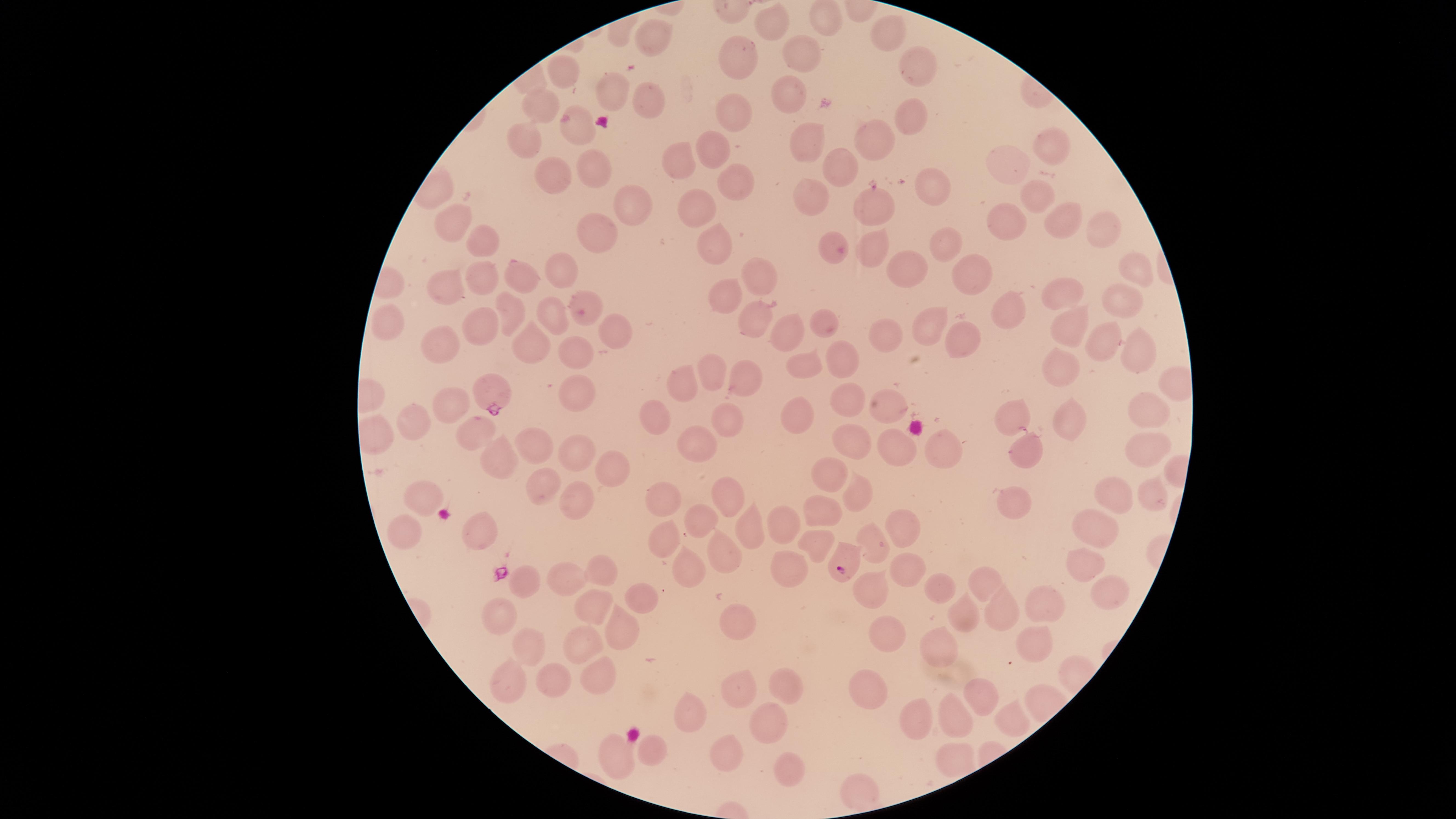

Approximate marker points as (x, y) in pixels. Uninfected red blood cells: (824, 21), (772, 27), (889, 35), (653, 37), (804, 59), (742, 61), (917, 64), (564, 77), (616, 93), (793, 100), (650, 102), (546, 106), (736, 115), (916, 119), (525, 135), (866, 135), (578, 136), (814, 141), (1050, 143), (715, 144), (681, 157), (838, 163), (1012, 164), (549, 167), (594, 167), (733, 179), (934, 185), (1036, 195), (628, 200), (812, 200), (704, 207), (881, 208), (1054, 217), (1008, 219), (457, 224), (1097, 231), (602, 232), (481, 239), (946, 239), (710, 245), (830, 249), (871, 249), (1140, 262), (909, 270), (565, 271), (973, 274), (526, 276), (753, 276), (480, 277), (449, 282), (728, 293), (1128, 294), (1064, 296), (582, 305), (512, 312), (1004, 313), (542, 316), (756, 320), (825, 323), (922, 324), (392, 326), (1068, 326), (474, 329), (613, 329), (783, 330), (963, 332), (884, 339), (1099, 340), (440, 341), (529, 346), (1132, 352), (581, 355), (845, 361), (810, 366), (1055, 373), (711, 374), (747, 376), (688, 387), (579, 395), (851, 397), (885, 405), (453, 409), (1152, 409), (799, 413), (659, 417), (1013, 419), (725, 421), (1066, 423), (417, 428), (475, 431), (850, 440), (938, 442), (698, 445), (1144, 446), (534, 449), (1026, 449), (576, 451), (898, 452), (501, 460), (609, 467), (835, 472), (728, 484), (543, 487), (866, 492), (1154, 494), (1112, 495), (581, 496), (423, 501), (662, 503), (826, 511), (1013, 511), (781, 522), (1100, 525), (702, 527), (482, 528), (750, 530), (405, 532), (898, 532), (885, 544), (821, 546), (668, 547), (726, 561), (1085, 562), (796, 567), (911, 568), (595, 571), (568, 575), (527, 576), (980, 579), (693, 582), (874, 586), (1116, 588), (948, 590), (636, 594), (1050, 601), (592, 609), (1006, 610), (965, 611), (503, 616), (746, 624), (882, 629), (624, 631), (1033, 642), (529, 645), (583, 647), (943, 653), (599, 676), (555, 677), (509, 679), (740, 684), (866, 688), (779, 689), (976, 693), (924, 717), (957, 717), (688, 722), (1013, 724), (770, 726), (726, 750), (652, 752), (615, 757), (790, 772), (856, 783), (856, 784). Parasitized red blood cells: (492, 391), (844, 560). The visible region is circular. Presence: malaria parasites seen. Single field of view. Thin blood smear. Giemsa stain. Species: Plasmodium falciparum. Image is 1456×819 pixels. Photographed with a smartphone camera through the microscope eyepiece.